State the preparation type.
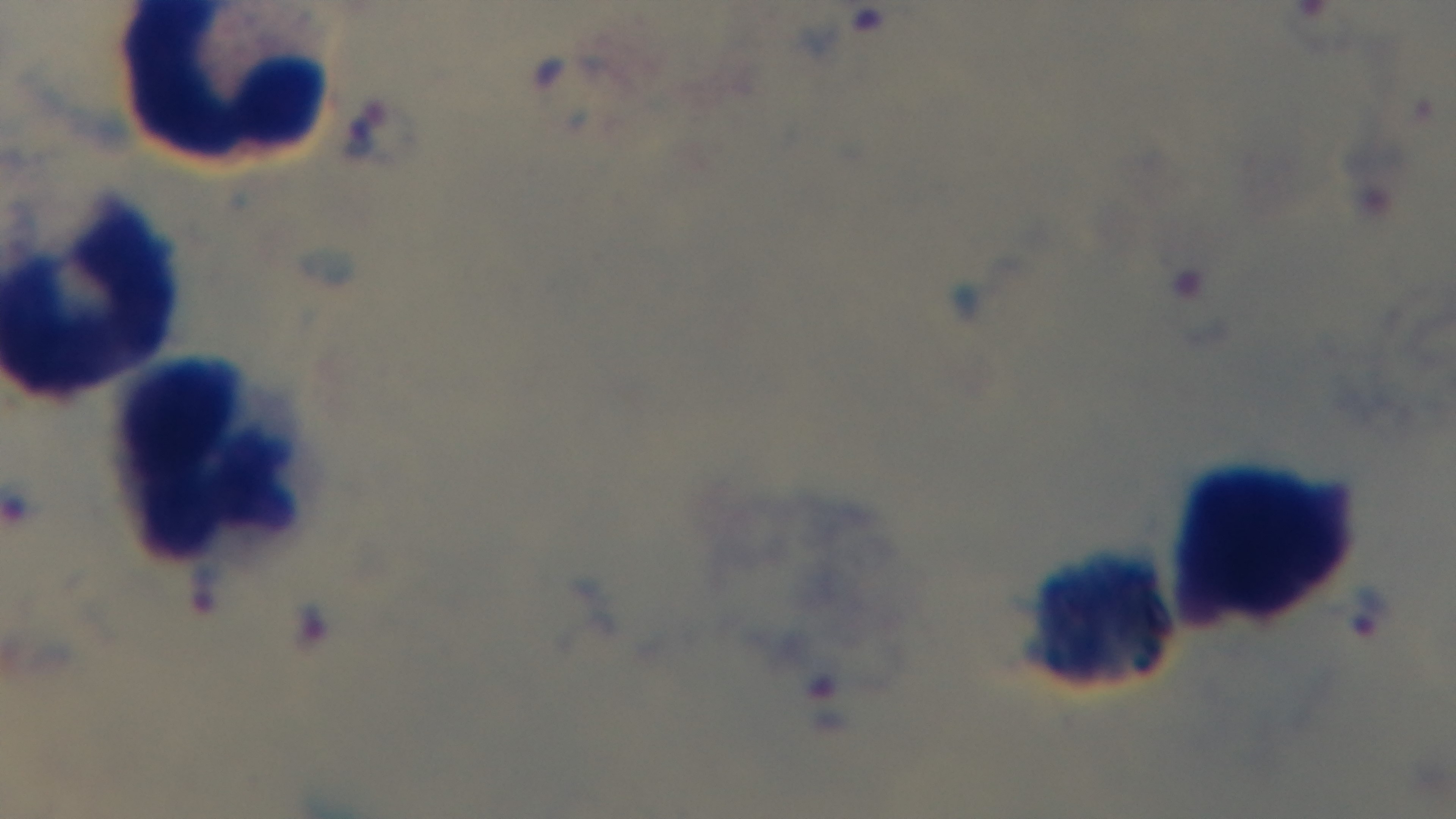
A thick smear.

One field from the slide. Giemsa-stained. Mounted 4K digital camera. Oil-immersion objective, 100x. Photomicrograph. Malaria status: infected.